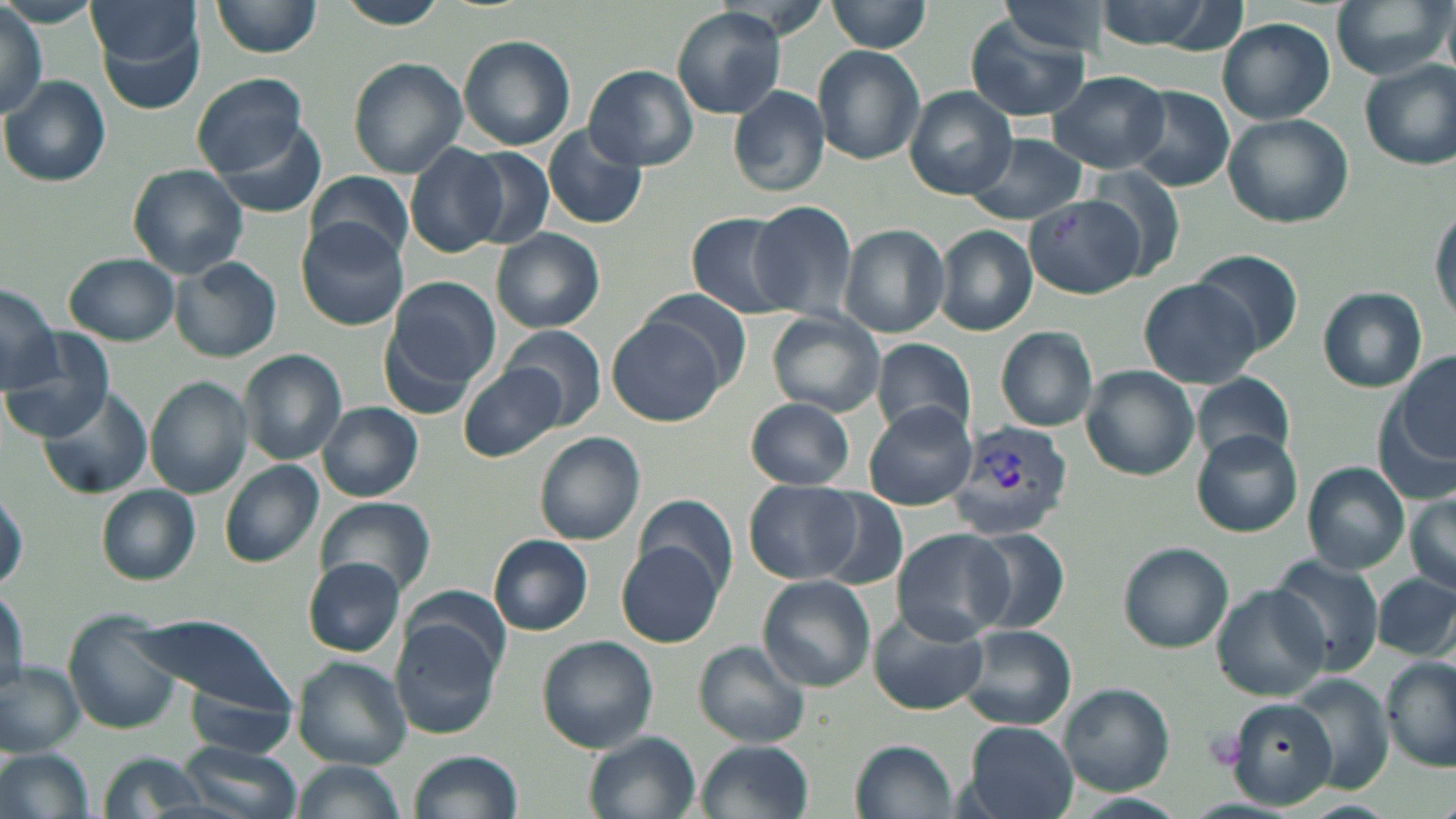
Approximate bounding boxes as (x1, y1, x2, y2) in pixels. Plasmodium vivax-infected red blood cell locations: (948, 420, 1074, 538). Uninfected red blood cell locations: (86, 0, 199, 69), (333, 0, 450, 29), (1088, 0, 1237, 51), (1331, 0, 1450, 80), (209, 1, 321, 59), (828, 1, 932, 53), (995, 2, 1110, 56), (0, 5, 45, 115), (671, 7, 788, 118), (1441, 7, 1456, 82), (95, 13, 208, 117), (967, 17, 1092, 122), (1218, 17, 1335, 124), (457, 35, 576, 150), (812, 46, 925, 165), (346, 57, 467, 177), (1360, 58, 1456, 170), (584, 66, 699, 171), (1047, 71, 1170, 173), (191, 74, 313, 178), (0, 76, 112, 185), (728, 85, 831, 196), (1122, 85, 1236, 192), (906, 87, 1017, 199), (1222, 113, 1353, 228), (209, 117, 328, 220), (541, 124, 649, 231), (964, 133, 1088, 225), (404, 143, 509, 257), (462, 148, 554, 249), (127, 163, 248, 279), (1086, 166, 1189, 280), (306, 170, 415, 265), (1024, 192, 1150, 299), (1430, 199, 1455, 329), (750, 201, 860, 319), (684, 211, 798, 319), (295, 219, 409, 331), (840, 224, 949, 338), (934, 226, 1038, 336), (491, 229, 605, 332), (1191, 249, 1306, 359), (64, 254, 181, 347), (170, 257, 281, 363), (385, 275, 501, 389), (1139, 278, 1261, 387), (0, 283, 61, 393), (1317, 287, 1427, 392), (644, 288, 752, 383), (766, 311, 883, 417), (609, 317, 726, 427), (507, 325, 608, 429), (995, 326, 1099, 431), (379, 329, 477, 421), (4, 330, 114, 441), (873, 338, 976, 440), (238, 349, 347, 465), (1394, 352, 1455, 461), (459, 362, 564, 459), (1081, 367, 1197, 478), (1191, 373, 1298, 467), (146, 376, 254, 498), (37, 385, 153, 498), (745, 398, 857, 490), (317, 402, 423, 502), (863, 404, 978, 509), (534, 431, 646, 545), (1191, 431, 1302, 538), (219, 461, 324, 569), (1301, 462, 1409, 574), (745, 482, 864, 584), (96, 485, 201, 584), (1404, 488, 1456, 597), (812, 491, 908, 593), (636, 494, 735, 595), (318, 498, 435, 597), (892, 527, 1016, 644), (961, 527, 1071, 635), (489, 535, 592, 635), (617, 542, 724, 648), (1118, 543, 1232, 652), (1271, 555, 1384, 675), (302, 559, 404, 656), (1372, 573, 1455, 659), (758, 576, 875, 692), (0, 584, 27, 695), (1211, 586, 1330, 700), (64, 610, 183, 737), (868, 611, 990, 715), (131, 614, 292, 714), (392, 619, 503, 738), (958, 624, 1076, 730), (535, 635, 658, 753), (694, 641, 809, 746), (292, 656, 412, 769), (1383, 656, 1456, 770), (0, 663, 83, 754), (1285, 676, 1395, 793), (1059, 685, 1173, 796), (186, 686, 293, 759), (1227, 698, 1341, 805), (963, 722, 1078, 819), (585, 732, 701, 819), (177, 737, 304, 819), (697, 739, 815, 819), (850, 739, 959, 819), (1, 748, 95, 819), (98, 750, 209, 818), (407, 750, 525, 819), (289, 759, 406, 819), (1072, 794, 1187, 819). Slide-level diagnosis: Plasmodium vivax. Thin blood film. May-Grünwald-Giemsa-stained preparation. Image is 1456×819 pixels. Captured at 1000x magnification. Optical microscopy. One field of a larger specimen.